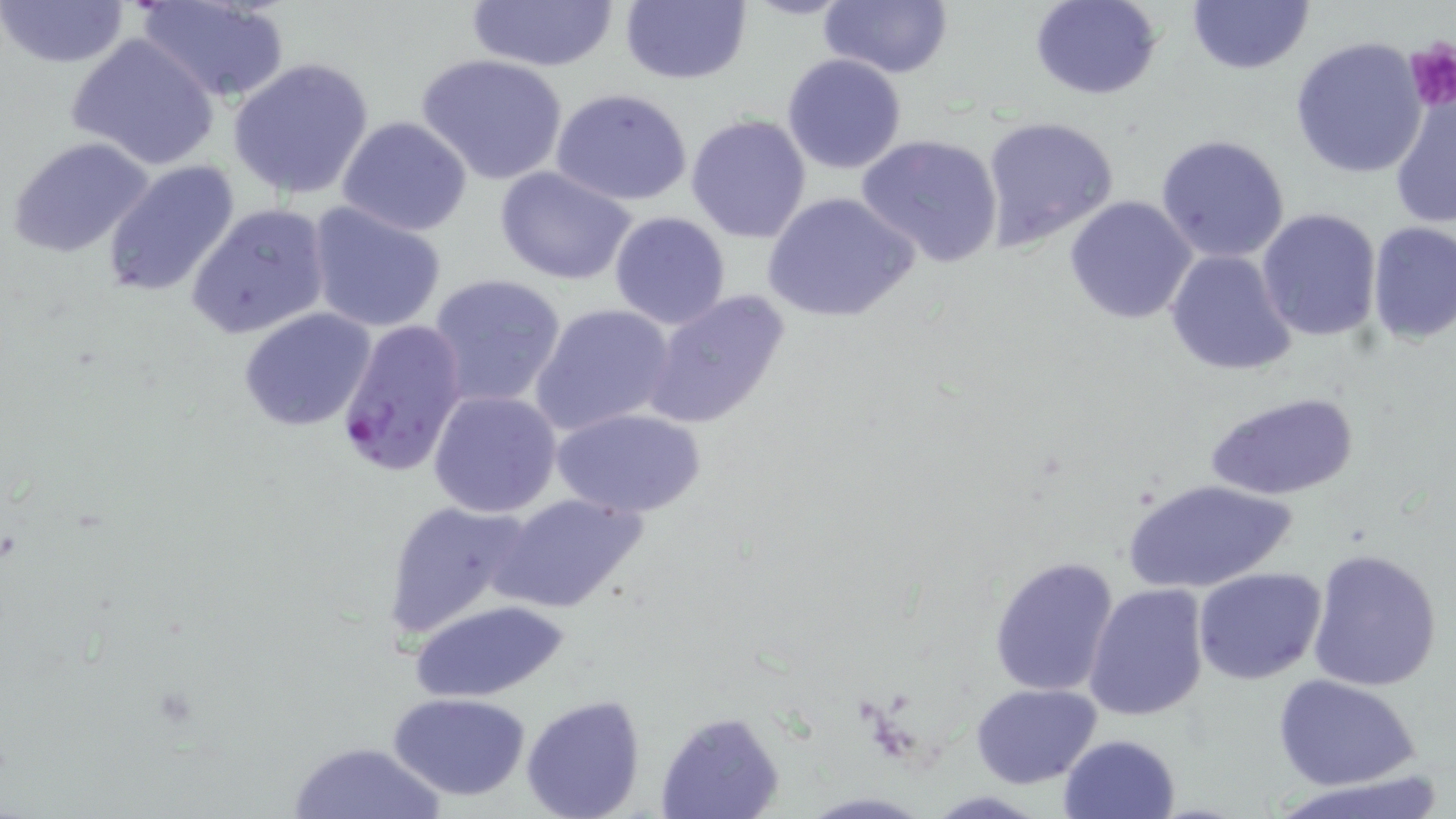
slide_level_diagnosis: Plasmodium falciparum
magnification: 1000x
modality: optical microscopy
image_size: 1456×819 pixels
preparation: thin blood film
stain: May-Grünwald-Giemsa
field_of_view: single
plasmodium_falciparum_infected_red_blood_cell_locations: 'approximate bounding boxes as [x1, y1, x2, y2] in pixels: [334, 318, 468, 480]'
uninfected_red_blood_cell_locations: 'approximate bounding boxes as [x1, y1, x2, y2] in pixels: [0, 0, 132, 70], [137, 0, 289, 105], [463, 0, 623, 71], [619, 0, 751, 86], [1030, 0, 1164, 100], [1186, 0, 1313, 75], [818, 1, 953, 79], [66, 34, 222, 172], [1290, 36, 1428, 179], [416, 53, 569, 185], [781, 53, 908, 174], [228, 57, 376, 200], [1390, 87, 1455, 232], [551, 88, 696, 207], [686, 114, 814, 244], [336, 116, 474, 238], [980, 116, 1121, 252], [855, 132, 1004, 267], [1156, 133, 1292, 264], [8, 135, 158, 258], [101, 160, 242, 301], [494, 164, 639, 285], [764, 190, 920, 325], [1062, 194, 1198, 325], [306, 201, 448, 332], [186, 203, 332, 341], [1256, 206, 1383, 343], [607, 211, 731, 330], [1365, 221, 1456, 345], [1164, 249, 1298, 376], [428, 272, 567, 409], [643, 289, 792, 431], [530, 303, 678, 437], [238, 309, 377, 431], [430, 389, 563, 517], [1207, 390, 1359, 501], [550, 406, 706, 518], [1123, 477, 1297, 596], [492, 492, 648, 616], [380, 498, 537, 640], [1306, 548, 1444, 692], [988, 556, 1121, 698], [1192, 566, 1326, 684], [1083, 582, 1211, 722], [411, 600, 566, 702], [1274, 675, 1421, 790], [971, 683, 1102, 787], [389, 692, 531, 800], [520, 694, 647, 819], [656, 711, 784, 819], [1058, 734, 1182, 819], [287, 739, 445, 819], [1274, 773, 1451, 819]'
platelet_locations: 'approximate bounding boxes as [x1, y1, x2, y2] in pixels: [1404, 40, 1455, 111]'